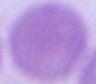
Micrograph. A red blood cell is seen. 1000x magnification.